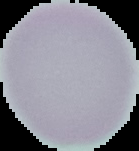 Image is 139×151 pixels. Segmented cell region on a black background. From a thin blood film. Result: negative for Plasmodium parasites.